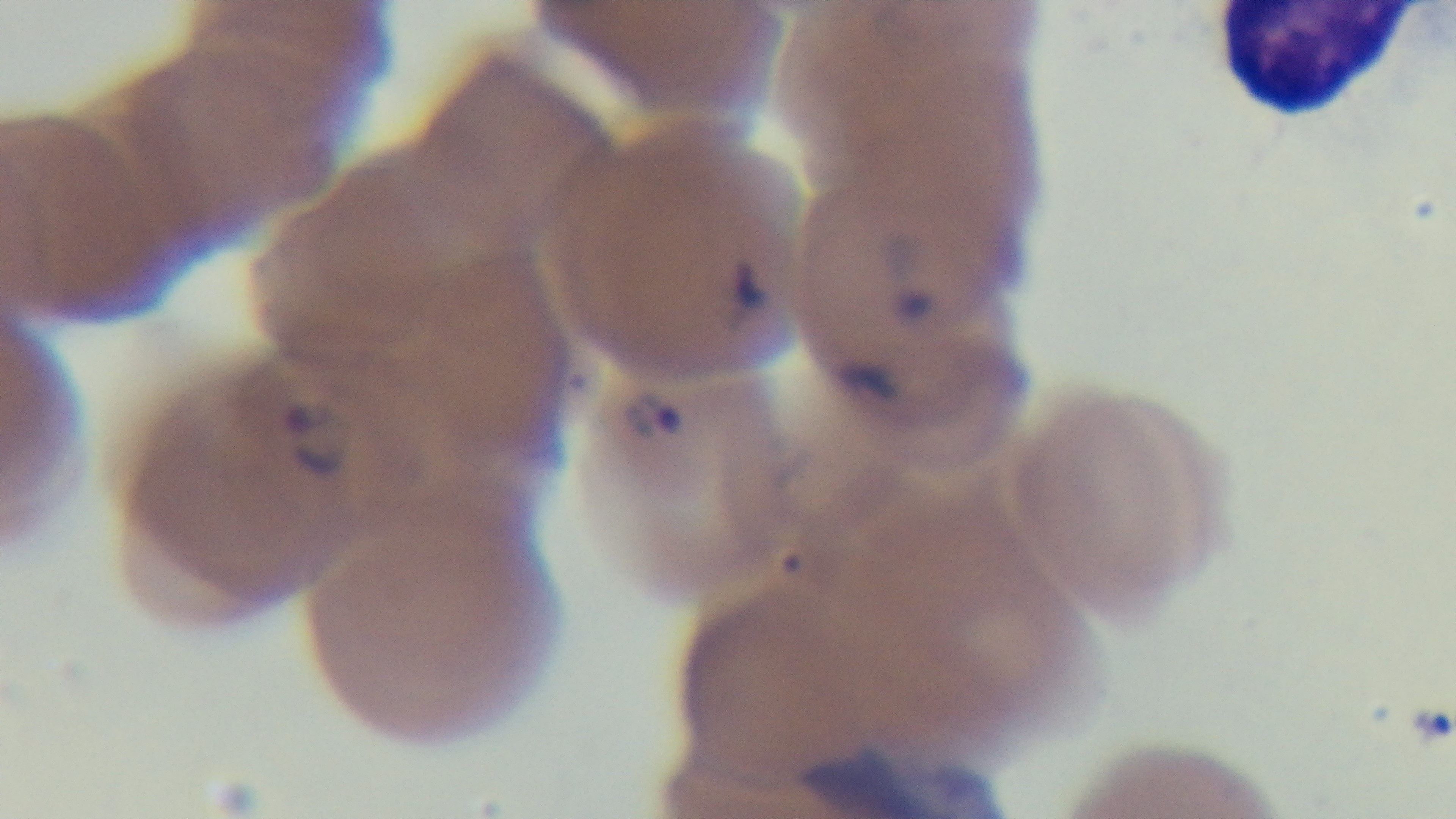

capture = mounted 4K digital camera
objective = 100x oil immersion
modality = light microscopy
stain = Giemsa
preparation = thin
field of view = single
malaria status = infected